Name the cell type shown.
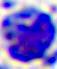
This is a leukocyte.

{
  "modality": "micrograph",
  "magnification": "400x"
}